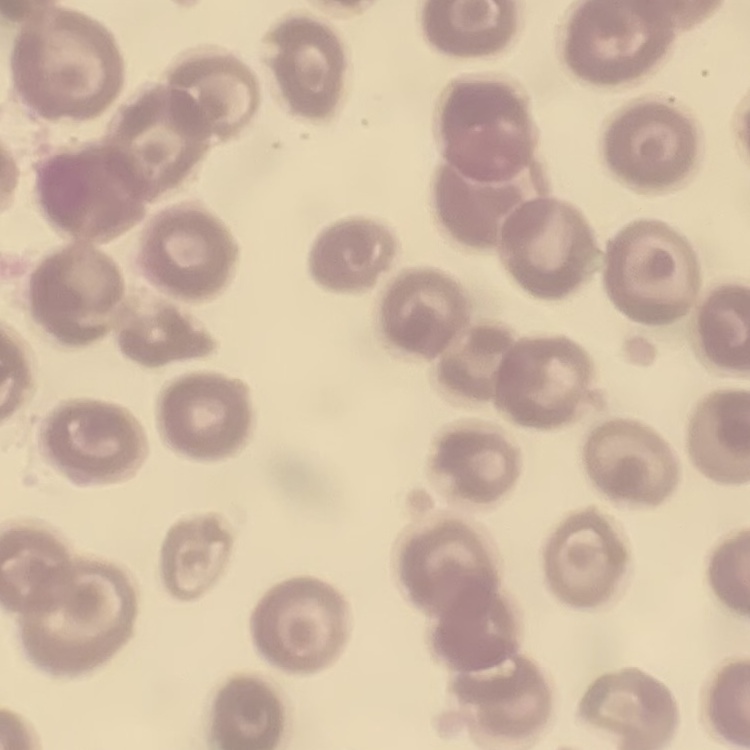
Summary:
  - Red blood cell morphology: no rouleaux formation
  - Image type: one tile cut from a larger photomicrograph
  - Preparation: thin peripheral smear
  - Stain: Field's or Giemsa